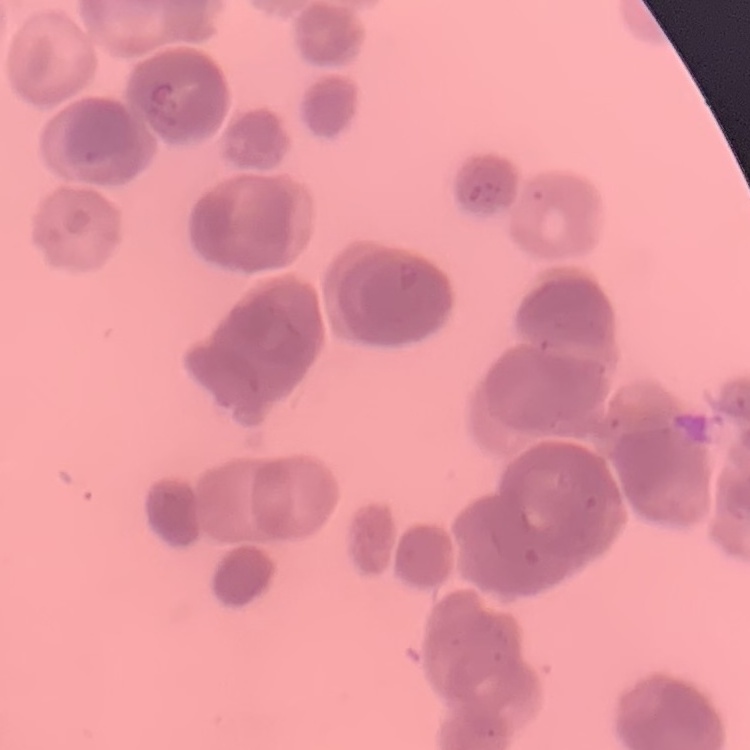

Summary:
  - Erythrocyte morphology: rouleaux formation
  - Preparation: thin blood film
  - Stain: Field's or Giemsa
  - Image type: square crop of a larger photomicrograph